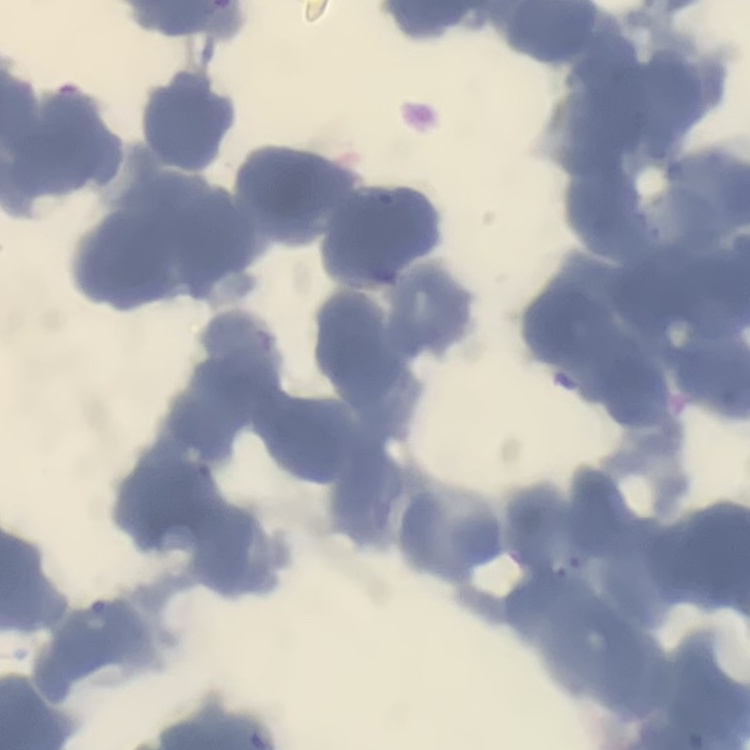
The erythrocytes show rouleaux formation. Thin peripheral smear. Stained with either Field's or Giemsa. One tile cut from a larger photomicrograph.